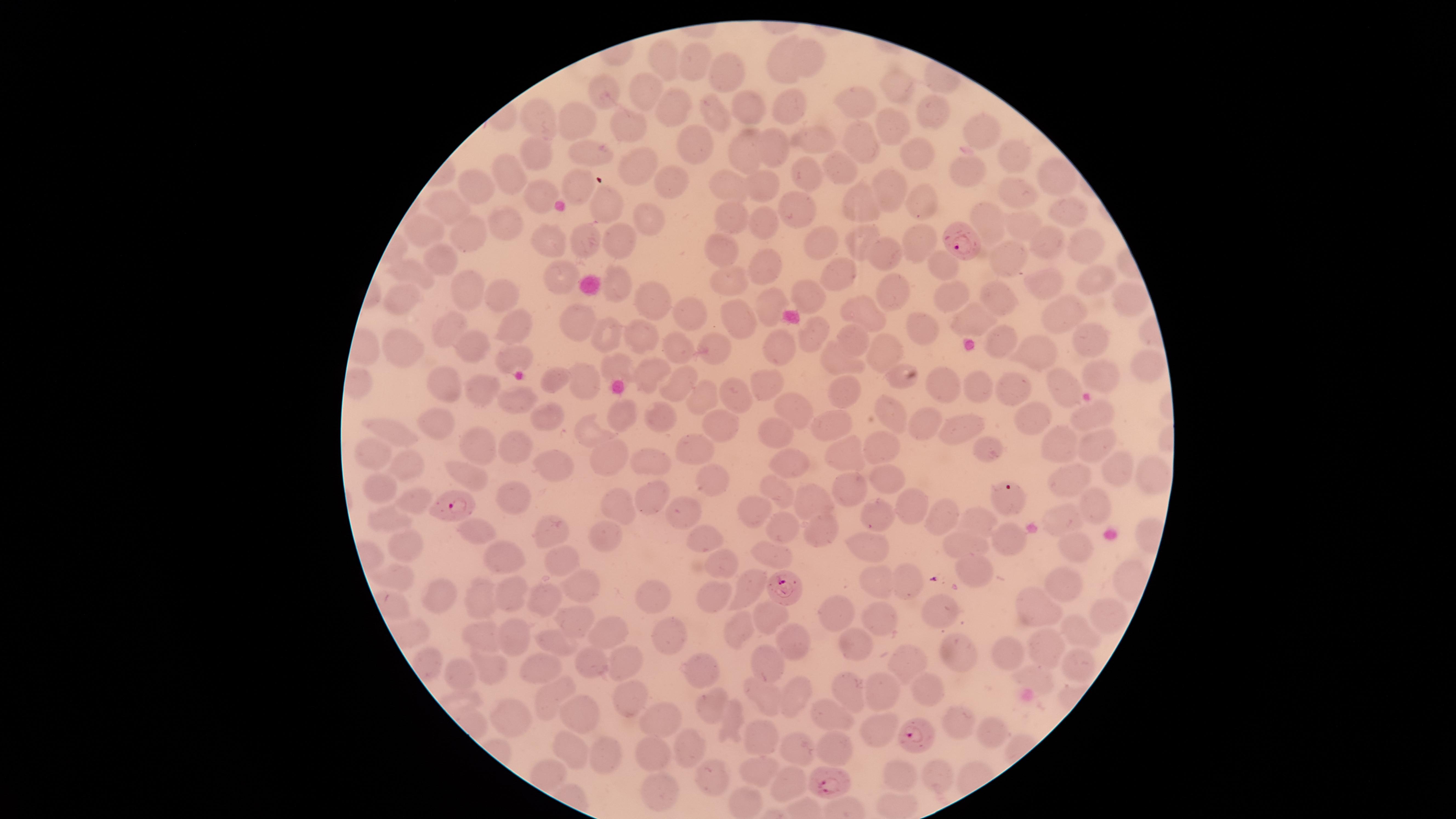

Approximate marker points as [x, y] in pixels.
Summary:
  - Parasitized RBCs: [964, 239], [1006, 496], [448, 508], [784, 588], [917, 734], [830, 777]
  - Uninfected RBCs: [814, 57], [779, 58], [668, 61], [692, 62], [726, 69], [896, 87], [643, 88], [607, 92], [858, 99], [787, 102], [746, 105], [673, 107], [929, 113], [715, 116], [537, 117], [577, 117], [628, 118], [892, 124], [981, 129], [816, 139], [857, 141], [689, 142], [772, 143], [592, 146], [744, 146], [911, 150], [1010, 150], [541, 152], [637, 162], [840, 166], [798, 172], [965, 172], [1050, 176], [510, 179], [726, 182], [577, 183], [665, 183], [887, 185], [765, 186], [477, 190], [1019, 192], [539, 195], [918, 197], [603, 200], [862, 202], [445, 207], [795, 208], [1066, 208], [985, 217], [733, 218], [506, 220], [647, 221], [1013, 221], [760, 224], [417, 229], [859, 232], [921, 235], [550, 236], [468, 238], [582, 238], [614, 238], [1084, 239], [1049, 241], [821, 242], [722, 249], [1015, 256], [438, 257], [883, 257], [770, 266], [943, 266], [412, 270], [836, 271], [566, 273], [1045, 278], [1094, 278], [727, 280], [617, 281], [469, 290], [806, 292], [898, 292], [501, 294], [1124, 294], [949, 296], [996, 296], [651, 297], [405, 298], [764, 304], [861, 307], [687, 311], [1062, 315], [447, 320], [972, 320], [736, 321], [517, 324], [578, 326], [924, 327], [808, 329], [641, 333], [606, 334], [1083, 334], [1005, 335], [853, 338], [469, 346], [676, 347], [710, 347], [398, 349], [1027, 349], [782, 350], [885, 351], [513, 356], [840, 357], [1151, 361], [613, 362], [1107, 372], [645, 374], [679, 375], [555, 377], [896, 378], [937, 380], [769, 381], [584, 384], [977, 384], [448, 386], [1061, 386], [484, 388], [1015, 390], [845, 392], [733, 393], [513, 398], [702, 398], [893, 405], [792, 406], [619, 410], [1031, 414], [546, 415], [1087, 415], [660, 416], [439, 418], [926, 418], [719, 422], [963, 424], [386, 425], [837, 426], [774, 428], [588, 432], [1101, 438], [1057, 439], [880, 441], [476, 446], [985, 446], [695, 448], [844, 448], [515, 449], [365, 456], [613, 458], [402, 460], [555, 461], [651, 461], [792, 464], [1115, 467], [1148, 474], [469, 476], [882, 477], [710, 479], [1072, 481], [375, 486], [856, 489], [772, 493], [508, 496], [649, 498], [411, 500], [806, 501], [615, 504], [911, 504], [1086, 506], [682, 511], [759, 512], [875, 513], [945, 516], [975, 516], [381, 519], [1062, 522], [824, 524], [783, 525], [552, 530], [476, 532], [608, 535], [703, 537], [1008, 537], [410, 541], [1073, 541], [960, 545], [863, 546], [771, 552], [720, 558], [507, 559], [564, 559], [976, 571], [399, 574], [872, 577], [907, 579], [587, 584], [1063, 585], [753, 586], [716, 590], [508, 591], [438, 595], [661, 595], [547, 596], [486, 599], [1032, 606], [769, 611], [840, 612], [939, 612], [1101, 612], [872, 615], [573, 618], [606, 628], [664, 628], [732, 630], [1078, 630], [483, 638], [508, 638], [797, 642], [563, 643], [856, 643], [961, 650], [1044, 651], [585, 654], [617, 654], [1011, 654], [902, 658], [1081, 662], [771, 664], [489, 668], [545, 668], [706, 672], [1029, 678], [460, 680], [797, 690], [850, 692], [882, 692], [925, 692], [551, 693], [624, 693], [760, 696], [577, 702], [713, 703], [521, 715], [831, 717], [658, 720], [728, 721], [958, 725], [875, 727], [989, 735], [761, 739], [688, 746], [796, 746], [652, 749], [570, 751], [833, 752], [606, 755], [545, 771], [937, 771], [714, 774], [755, 774], [904, 778], [789, 784], [659, 786], [745, 803]
  - Visible region: circular
  - Species: Plasmodium falciparum
  - Image size: 1456×819 pixels
  - Capture: smartphone photograph through the microscope eyepiece
  - Preparation: thin blood film
  - Presence: malaria parasites identified
  - Field of view: single
  - Stain: Giemsa